Assess this cell for malaria.
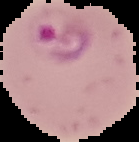

It is parasitized.

Summary:
  - Image size: 139×142 pixels
  - Image type: cell region segmented out of the field of view; surrounding area masked to black
  - Preparation: thin blood smear